Report the malaria status of this cell.
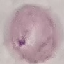
It is uninfected.

Giemsa stain. Thin smear of blood. Photographed with a smartphone camera at the microscope eyepiece. Automatically extracted cell patch, resized to 64 × 64 pixels.